Comment on the morphology of the erythrocytes.
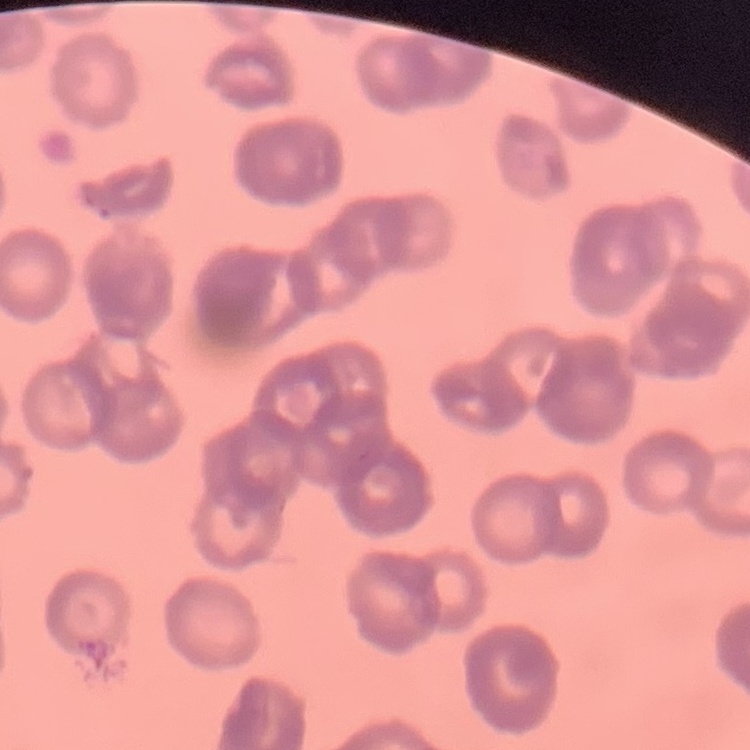

They show rouleaux formation.

image_type: square crop of a larger photomicrograph
preparation: thin blood smear
stain: Field's or Giemsa